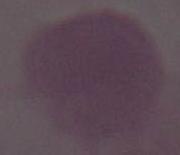 A red blood cell is shown. Captured at 1000x magnification. Photomicrograph.